Report the malaria status of this cell.
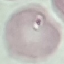

Uninfected.

Giemsa stain. Automatically extracted cell patch, resized to 64 × 64 pixels. Acquired by smartphone through the microscope eyepiece. Thin smear of blood.